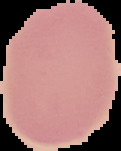
result = no Plasmodium parasites seen
preparation = thin blood film
image size = 121×151 pixels
image type = segmented cell region with the area outside set to black